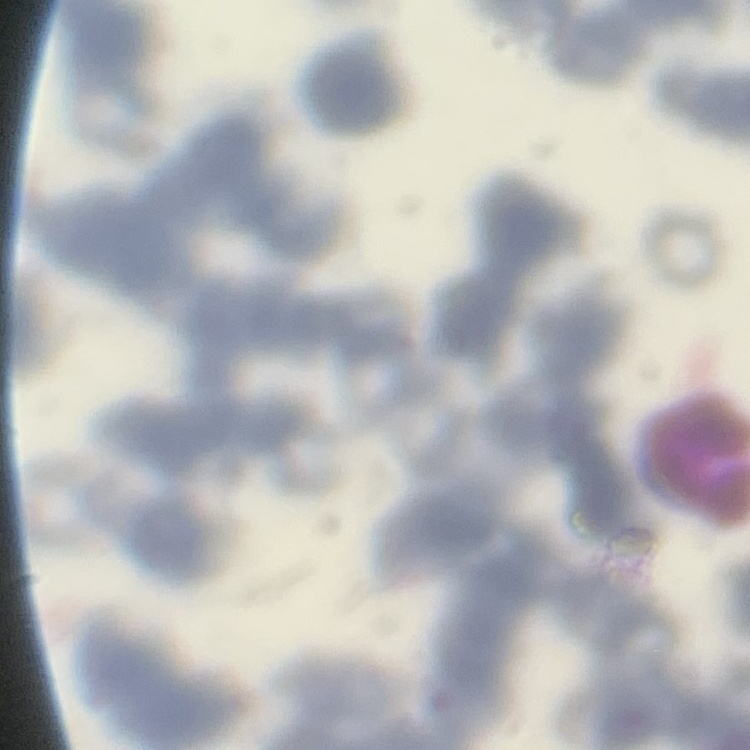

The red blood cells show rouleaux formation. Thin blood smear. One tile cut from a larger photomicrograph. Field's or Giemsa stain.